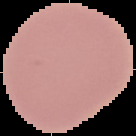

Cell region segmented out of the field of view; the surrounding area is masked to black. Image is 136×136 pixels. From a thin blood smear. Malaria status: uninfected.